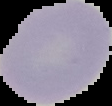

Summary:
  - Image size: 112×106 pixels
  - Result: no malaria parasites detected
  - Preparation: thin blood film
  - Image type: segmented cell region on a black background